Locate every malaria parasite and every leukocyte.
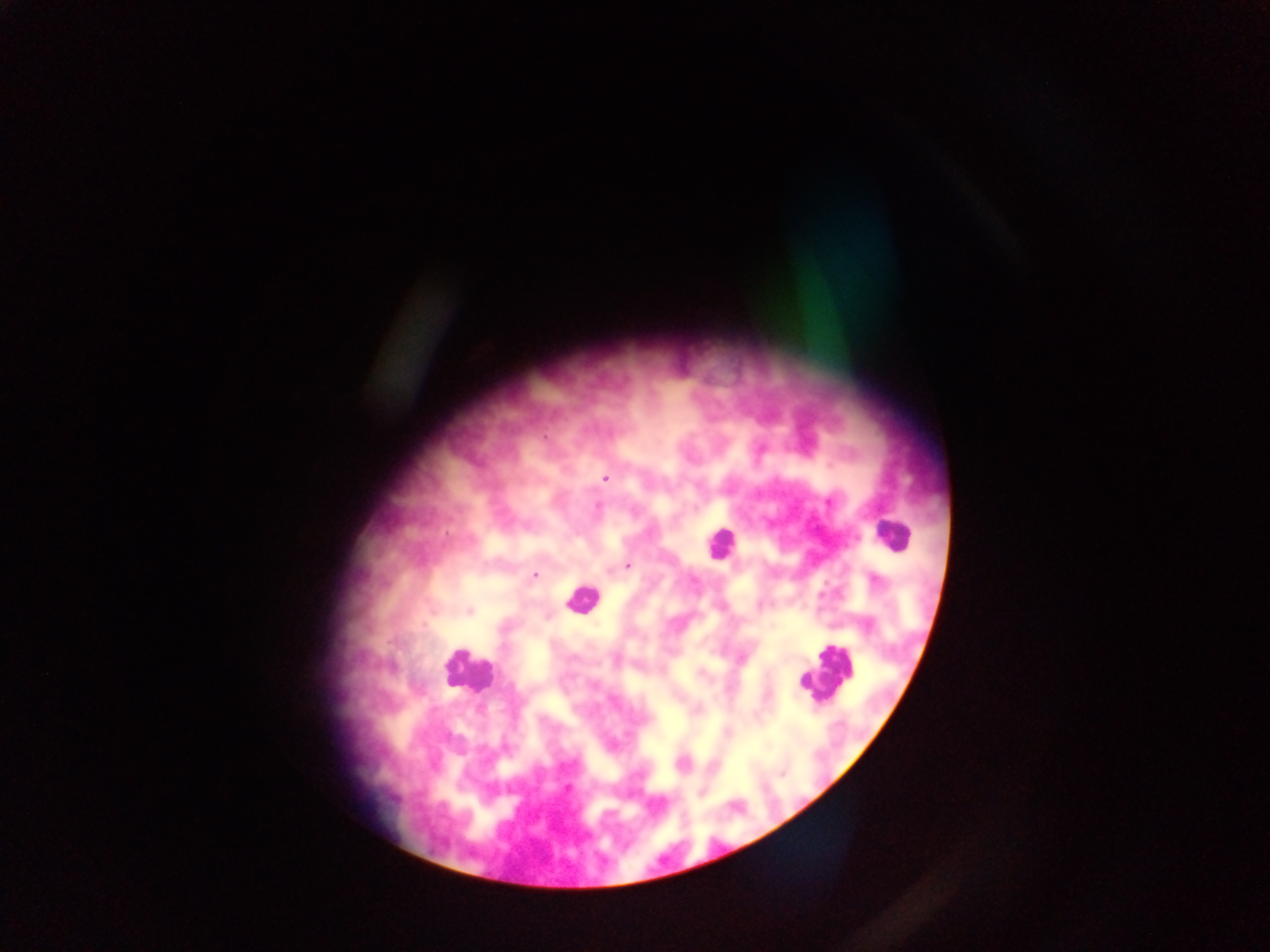
Approximate centers as [x, y] in pixels.
Malaria parasites: [605, 478], [828, 502], [599, 507], [628, 566], [536, 575], [876, 581], [469, 611], [782, 773], [567, 787].
Leukocytes: [891, 534], [719, 544], [580, 598], [467, 671], [826, 671].

Summary:
  - Capture: mobile-phone photograph through a microscope
  - Country: Ghana
  - Preparation: thick blood smear
  - Field of view: single
  - Image size: 1270×952 pixels